Identify the cell.
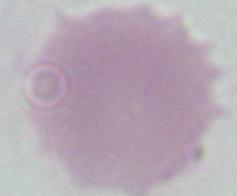

An erythrocyte.

Micrograph. 1000x magnification.